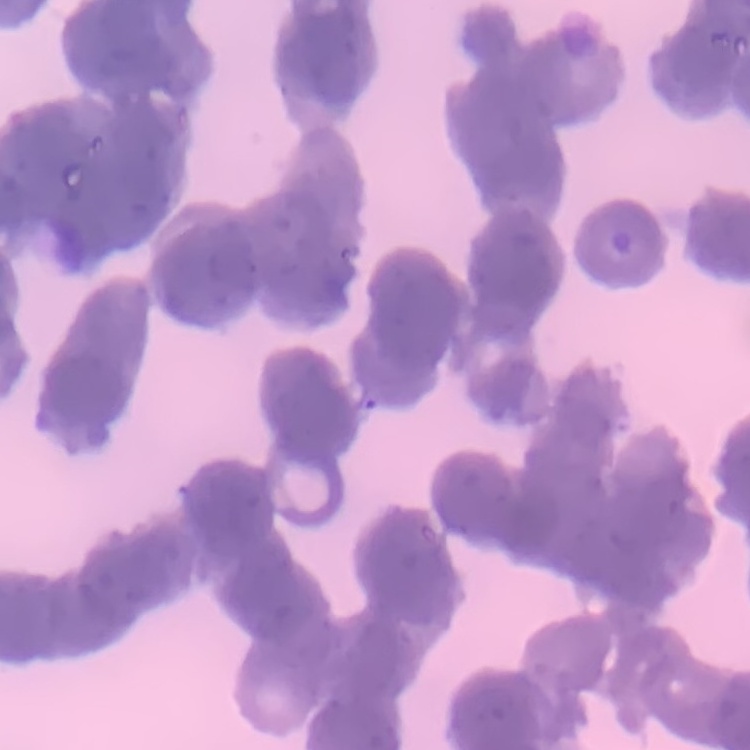

{
  "red_blood_cell_morphology": "rouleaux formation",
  "image_type": "one tile cut from a larger photomicrograph",
  "preparation": "thin blood smear",
  "stain": "Field's or Giemsa"
}